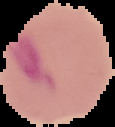
{
  "image_type": "segmented cell region with the area outside set to black",
  "result": "Plasmodium parasites detected",
  "preparation": "thin blood smear",
  "image_size": "115×127 pixels"
}